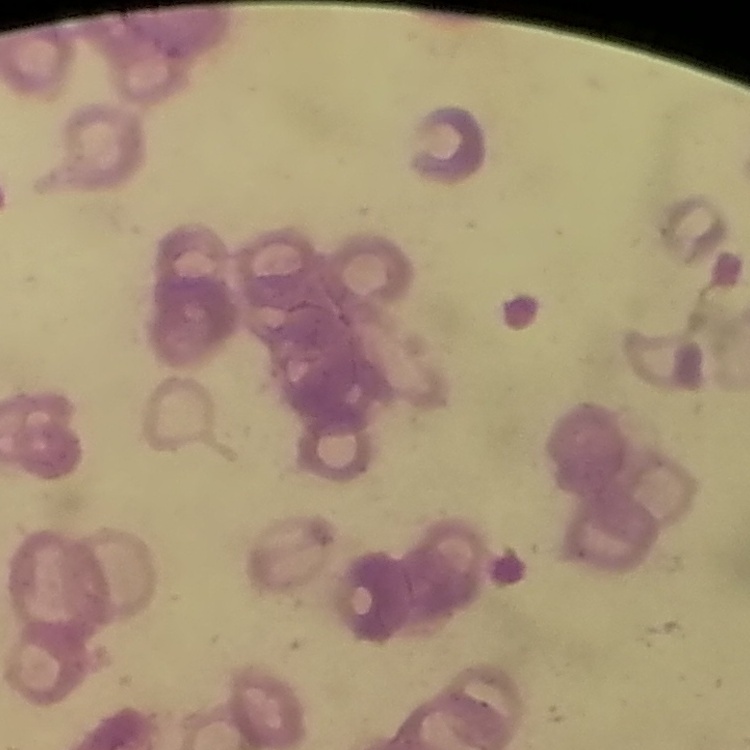 The red blood cells exhibit rouleaux formation. One tile cut from a larger photomicrograph. Stained with either Field's or Giemsa. Thin blood smear.